Name the parasite shown.
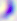
Toxoplasma gondii.

Summary:
  - Modality: micrograph
  - Magnification: 400x